Identify the blood parasite species.
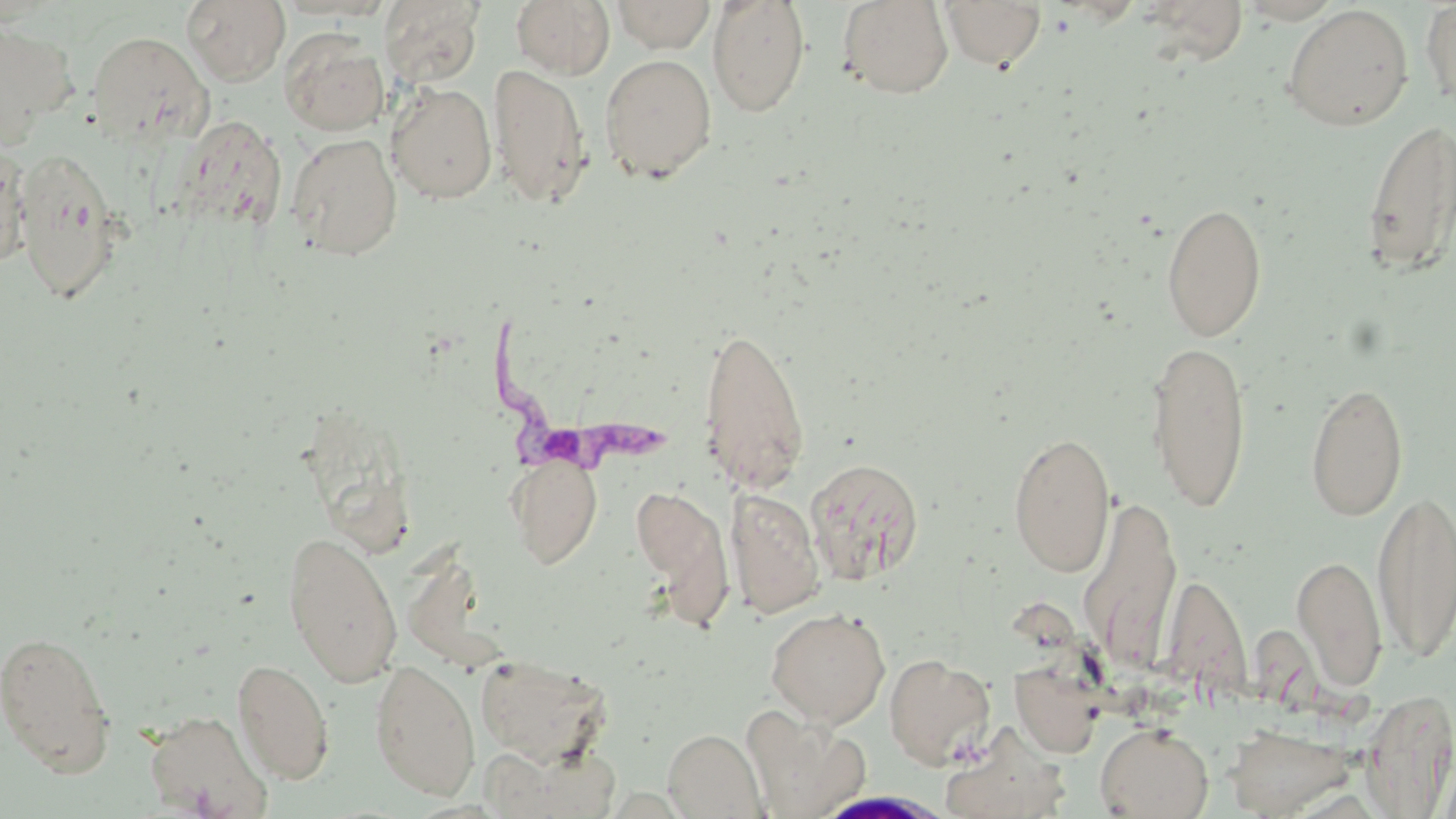
Trypanosoma brucei.

Approximate bounding boxes as (x1,y1)-(x2,y2) corner pairs in pixels. Trypanosoma brucei locations: (484,322)-(666,475). White blood cell locations: (815,790)-(954,818). Uninfected red blood cell locations: (183,0)-(290,86), (381,0)-(483,87), (511,0)-(616,79), (611,0)-(716,53), (707,0)-(811,117), (837,0)-(954,99), (940,0)-(1046,71), (1138,1)-(1250,66), (1420,1)-(1456,114), (1281,4)-(1414,131), (0,19)-(77,147), (279,30)-(389,136), (87,31)-(213,147), (599,53)-(718,184), (487,63)-(594,209), (387,82)-(497,203), (176,117)-(286,233), (1361,117)-(1456,277), (287,133)-(403,260), (0,144)-(32,269), (12,149)-(125,304), (1161,200)-(1267,342), (698,323)-(810,494), (1145,340)-(1252,511), (1305,380)-(1409,521), (1008,431)-(1116,578), (506,454)-(603,569), (804,457)-(925,584), (631,484)-(733,623), (726,487)-(825,618), (1372,488)-(1455,663), (1079,494)-(1183,671), (282,529)-(403,687), (1292,553)-(1387,692), (1164,573)-(1253,700), (766,607)-(891,728), (0,629)-(117,777), (474,654)-(611,765), (884,654)-(996,769), (372,657)-(602,786), (233,658)-(334,784), (370,659)-(480,800), (1010,660)-(1104,758), (1359,688)-(1456,817), (741,707)-(868,819), (143,710)-(273,818), (1095,723)-(1213,818), (1224,723)-(1357,818), (941,728)-(1072,819), (663,729)-(766,818), (488,745)-(618,817). One field of a larger specimen. Captured at 1000x magnification. May-Grünwald-Giemsa stain. Thin blood smear. Optical microscopy. Image is 1456×819 pixels.